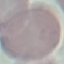
Summary:
  - Malaria status: uninfected
  - Stain: Giemsa
  - Capture: smartphone camera at the microscope eyepiece
  - Image type: automatically extracted cell patch, resized to 64 × 64 pixels
  - Preparation: thin blood film